Evaluate for malaria.
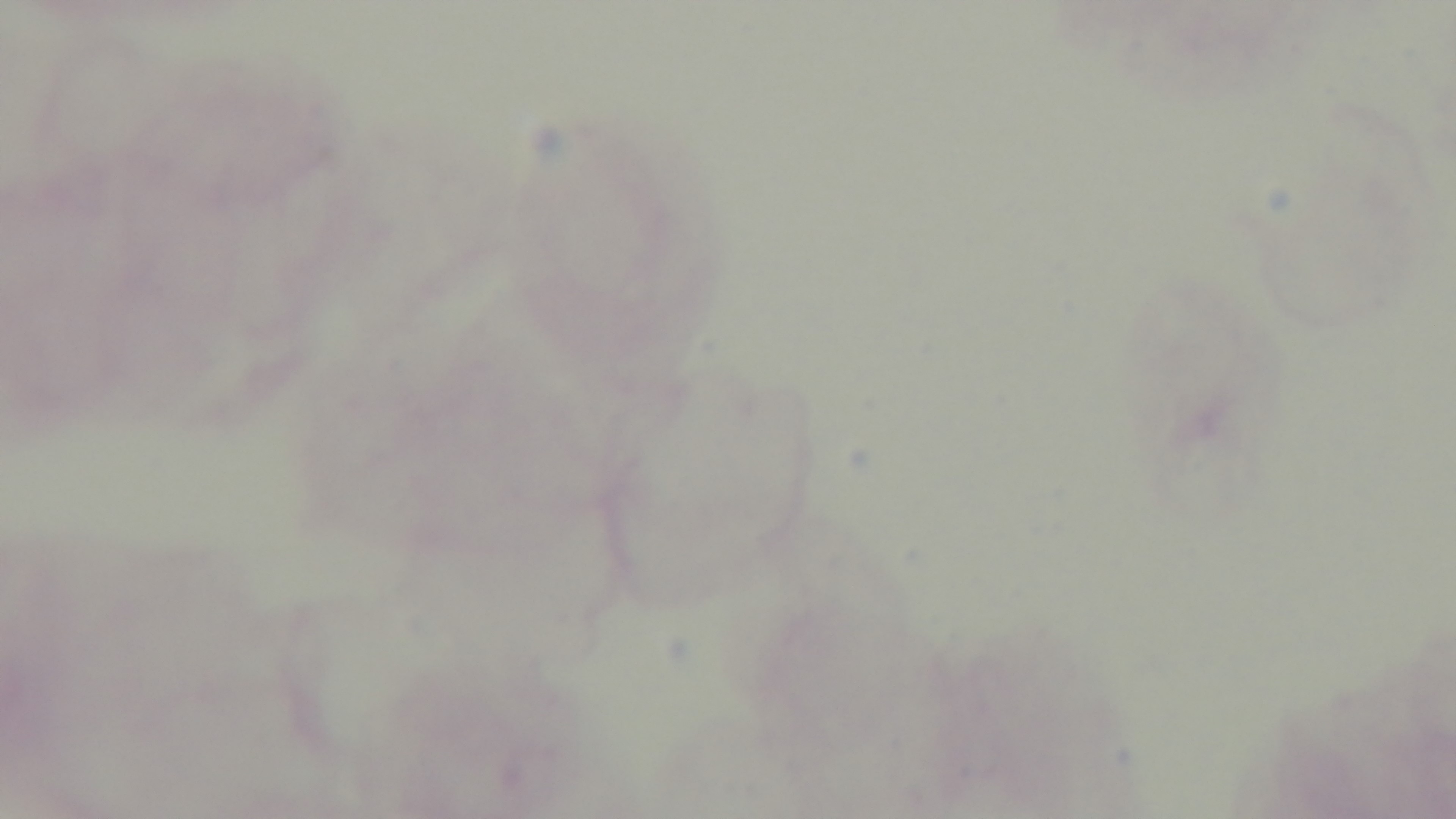
Uninfected.

Mounted 4K digital camera. Giemsa stain. Preparation: thick blood film. Photomicrograph. One field from the slide. Oil-immersion objective, 100x.